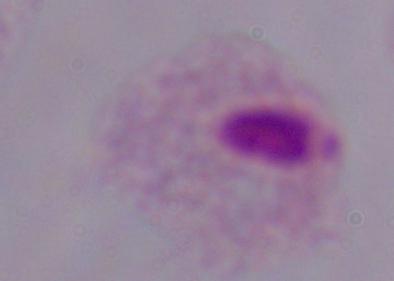
Summary:
  - Identification: trichomonad
  - Modality: micrograph
  - Magnification: 1000x